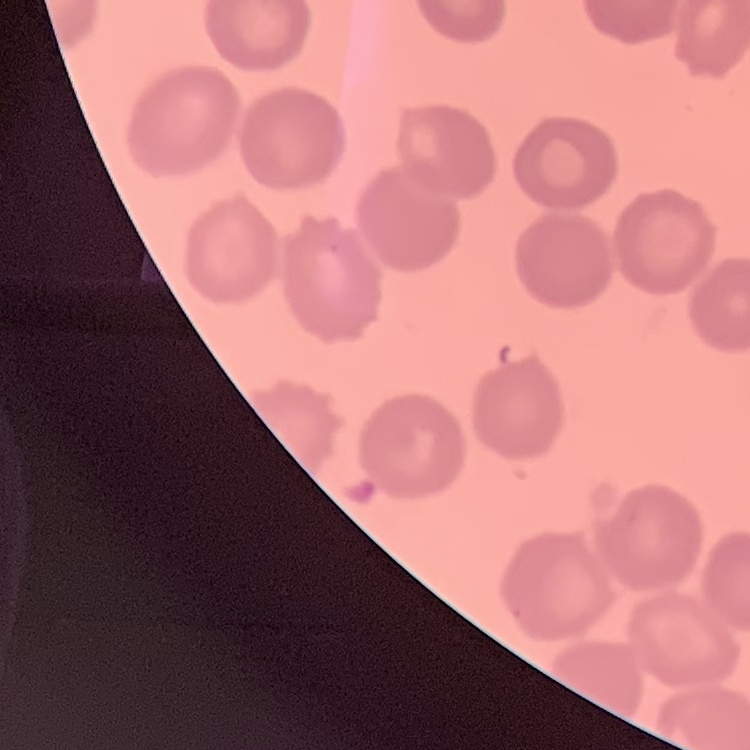
The erythrocytes exhibit no rouleaux formation. Thin blood film. Field's or Giemsa stain. One tile cut from a larger photomicrograph.